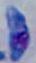
modality = micrograph
identification = Toxoplasma gondii
magnification = 1000x